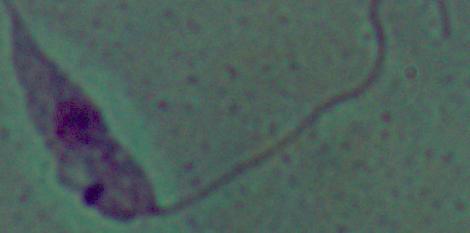

A Leishmania parasite is shown. Micrograph. Captured at 1000x magnification.